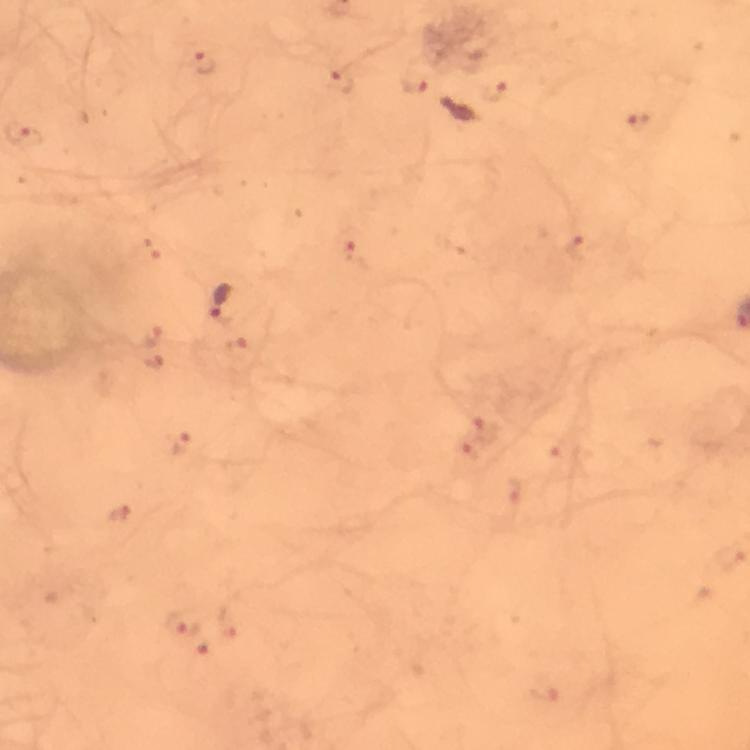

Approximate centers as {x, y} in pixels.
Summary:
  - Malaria parasite locations: {204, 63}, {342, 81}, {415, 85}, {494, 91}, {457, 112}, {638, 123}, {19, 134}, {577, 250}, {354, 252}, {220, 302}, {155, 338}, {154, 362}, {488, 428}, {180, 443}, {469, 448}, {513, 497}, {118, 515}, {228, 622}, {183, 623}, {202, 655}, {547, 689}
  - Immersion oil: applied
  - Capture: smartphone camera through the microscope
  - Cropped from: a single field of view
  - Context: from a diagnostic examination for malaria
  - Image size: 750×750 pixels
  - Stain: Giemsa
  - Preparation: thick smear
  - Magnification: 100x